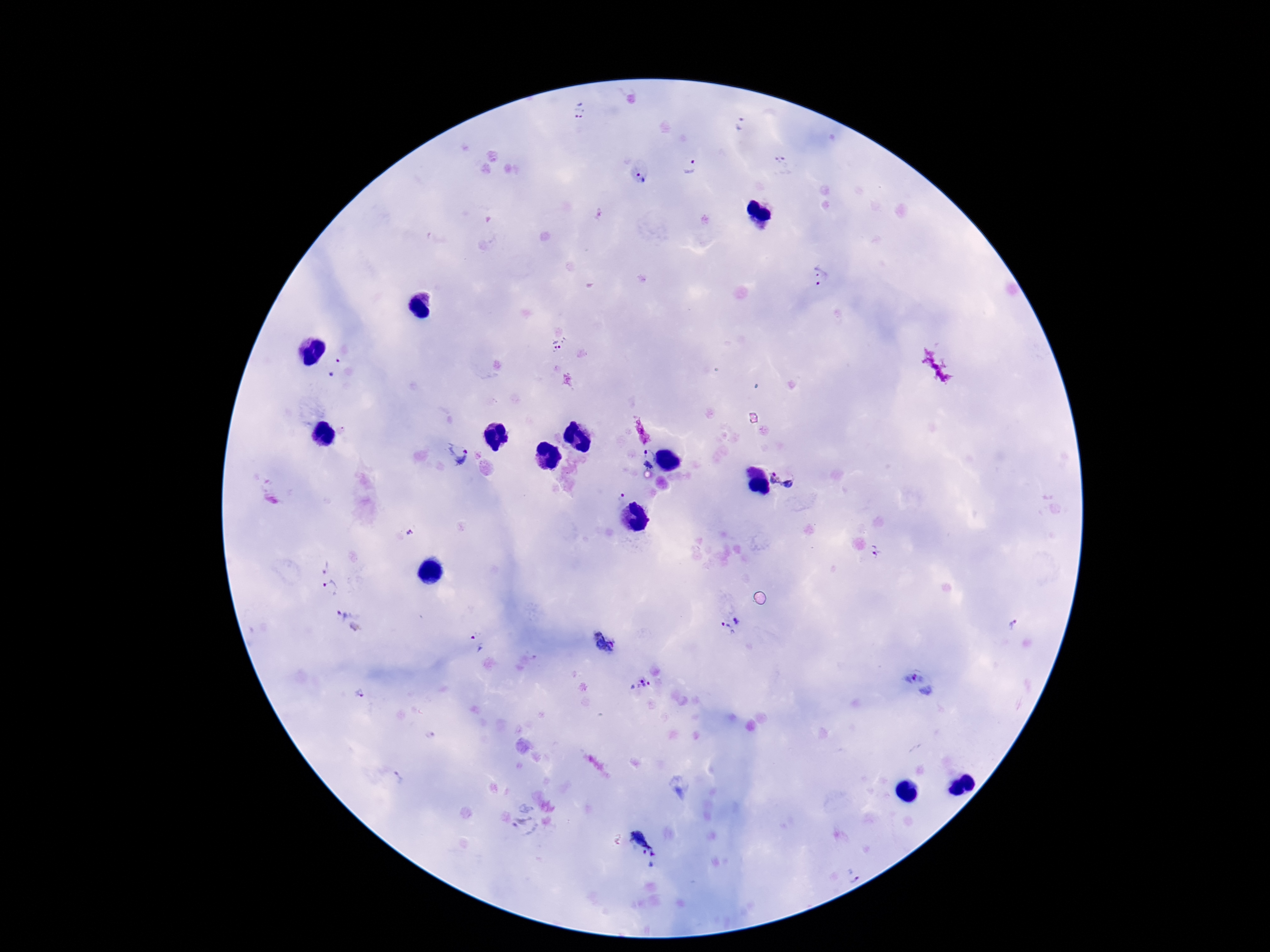

Approximate centers as {x, y} in pixels.
Summary:
  - Plasmodium parasite locations: {579, 110}, {741, 124}, {780, 159}, {690, 168}, {640, 177}, {821, 276}, {561, 346}, {334, 365}, {651, 453}, {458, 454}, {648, 465}, {777, 477}, {789, 484}, {621, 496}, {410, 532}, {878, 551}, {324, 564}, {330, 588}, {349, 620}, {737, 621}, {1013, 625}, {724, 627}, {475, 641}, {605, 643}, {640, 683}, {921, 683}, {360, 693}, {429, 736}, {400, 779}, {525, 819}, {648, 845}, {854, 876}
  - Capture: smartphone camera through the microscope eyepiece
  - Patient malaria status: infected
  - Field of view: single
  - Image size: 1270×952 pixels
  - Magnification: 100x
  - Stain: Giemsa
  - Preparation: thick blood film